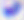
{
  "modality": "micrograph",
  "magnification": "400x",
  "identification": "Toxoplasma gondii"
}